Evaluate for malaria.
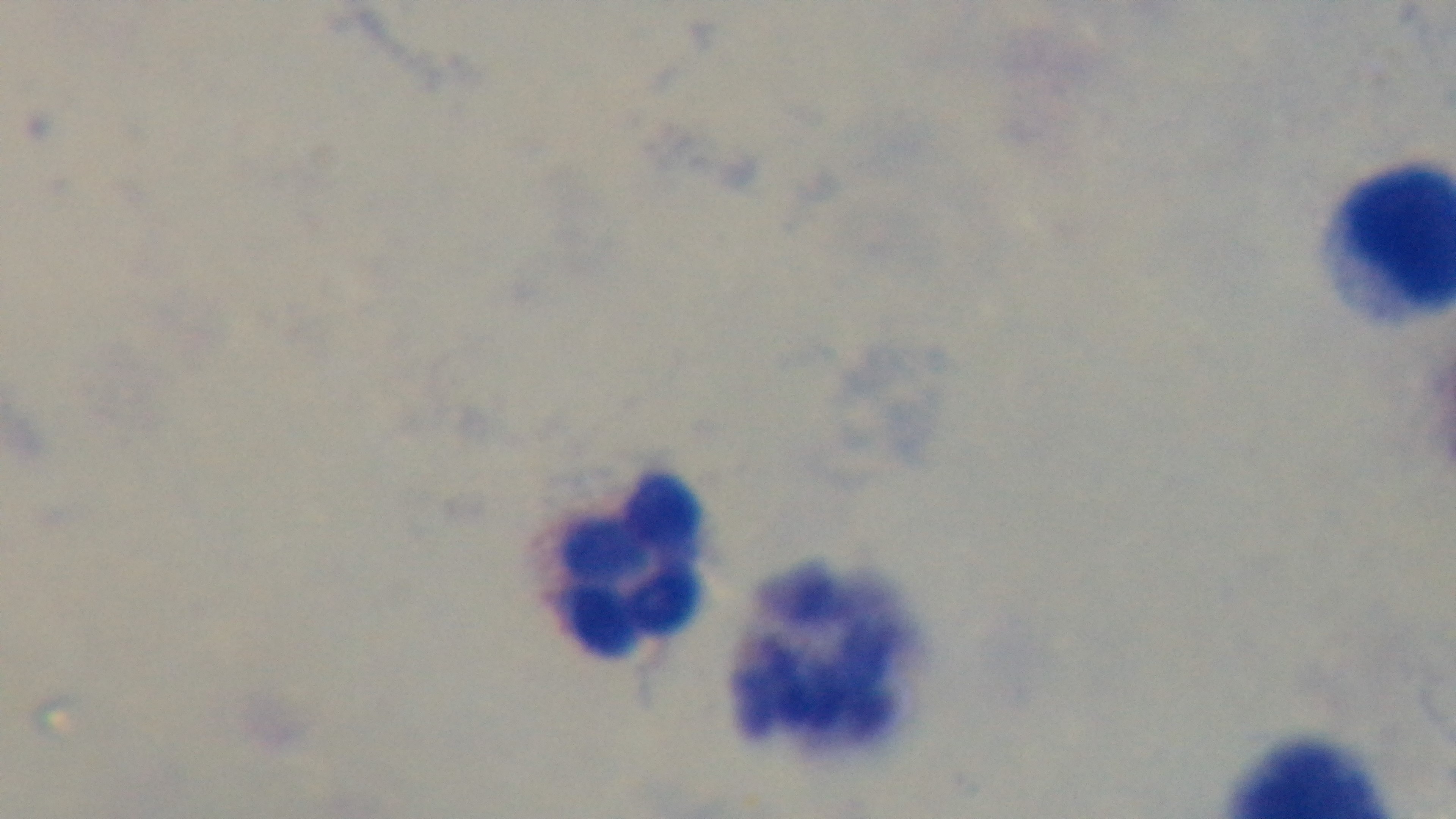
It is uninfected.

Captured with a mounted 4K digital camera. Giemsa stain. One field from the slide. Preparation: thick blood film. Oil-immersion objective, 100x. Light microscopy.